State which parasite is depicted.
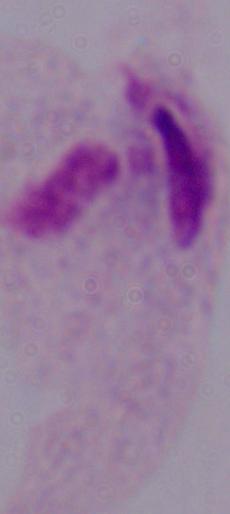

This is a trichomonad.

Summary:
  - Magnification: 1000x
  - Modality: micrograph